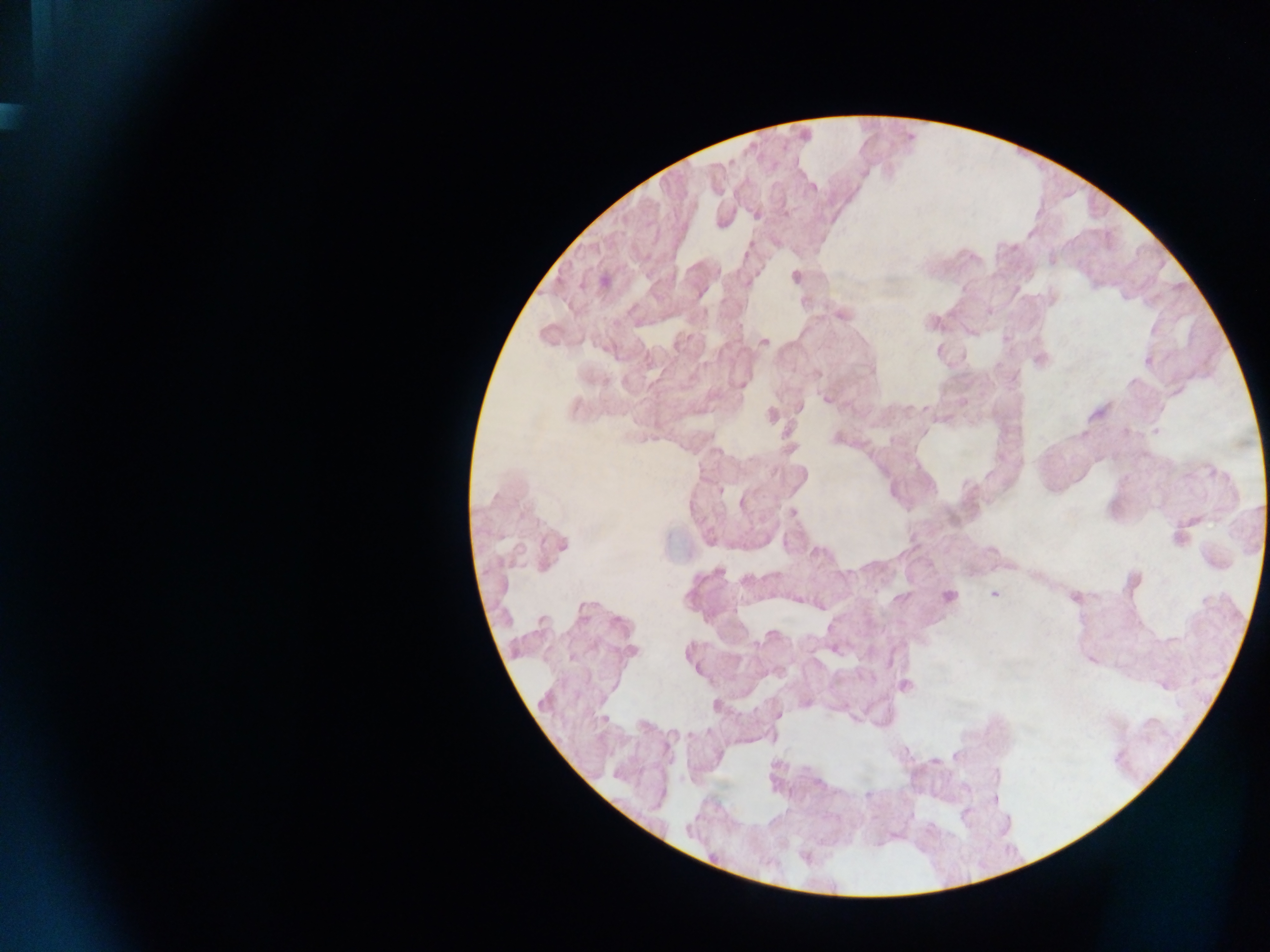

Approximate centers as x y in pixels. Malaria parasite locations: 947 595; 994 595. Single field of view. Collected in Ghana. Image is 1270×952 pixels. Thick blood smear. Photographed through a microscope with a mobile-phone camera.